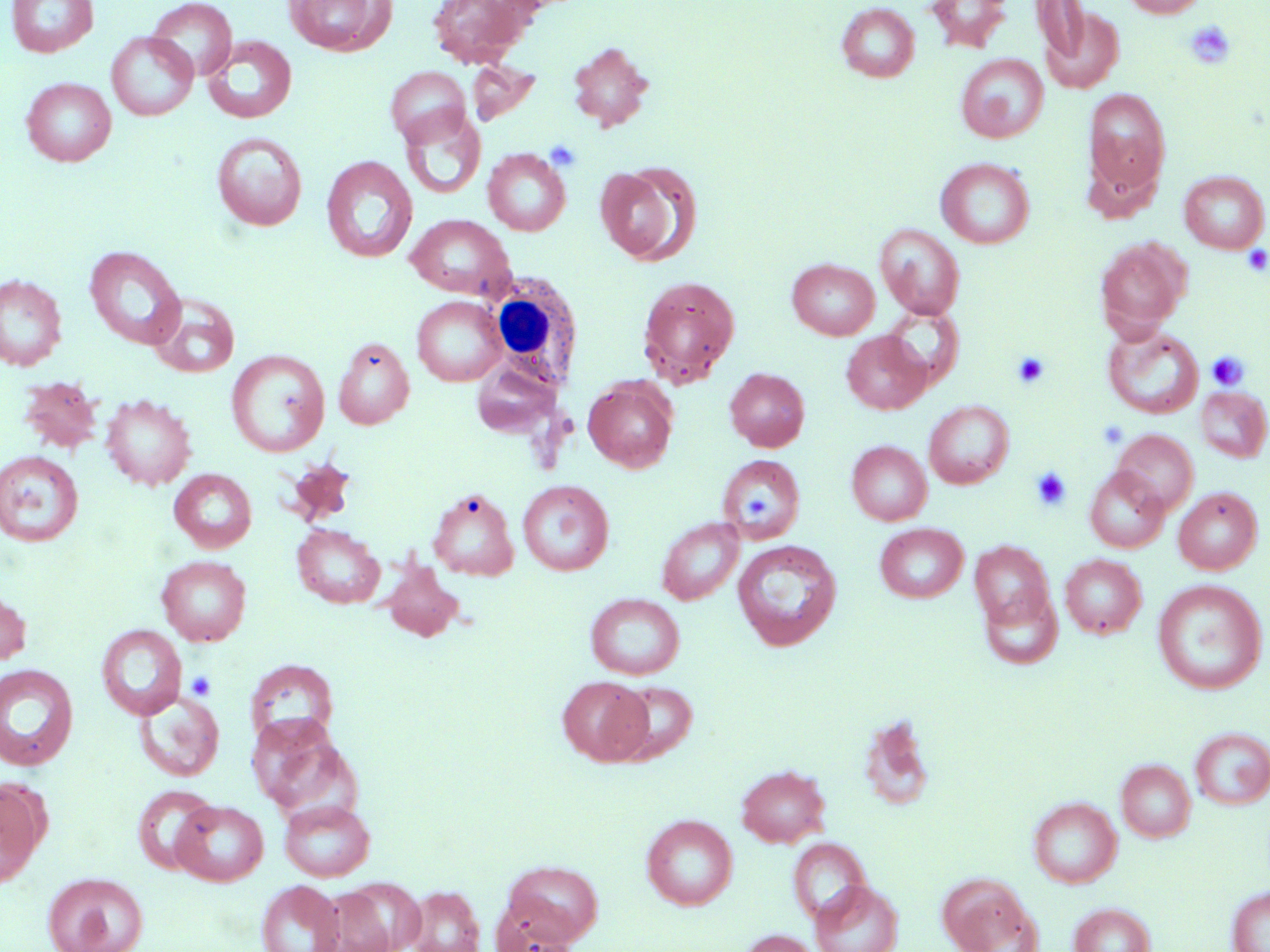

slide-level diagnosis = negative for blood parasites
preparation = thin blood film
white blood cell locations = approximate bounding boxes as (x1,y1)-(x2,y2) corner pairs in pixels: (478,269)-(584,391)
field of view = single
stain = May-Grünwald-Giemsa
uninfected red blood cell locations = approximate bounding boxes as (x1,y1)-(x2,y2) corner pairs in pixels: (6,0)-(98,57), (147,0)-(237,81), (284,0)-(395,56), (427,0)-(535,68), (926,0)-(1014,53), (1031,0)-(1091,64), (1123,0)-(1207,18), (836,2)-(920,82), (1037,4)-(1124,93), (106,32)-(198,121), (202,35)-(297,123), (567,41)-(654,132), (956,54)-(1048,143), (466,60)-(541,126), (385,66)-(471,147), (21,77)-(116,166), (1083,88)-(1171,203), (399,108)-(486,201), (211,132)-(307,231), (483,149)-(571,236), (321,156)-(417,263), (935,157)-(1035,248), (595,163)-(702,267), (1179,170)-(1269,253), (406,214)-(515,299), (875,224)-(965,320), (1095,239)-(1190,334), (84,245)-(186,350), (787,259)-(880,340), (0,274)-(66,370), (637,275)-(740,388), (148,294)-(240,378), (412,296)-(507,386), (881,304)-(965,388), (1103,324)-(1204,419), (842,331)-(931,414), (332,337)-(414,428), (226,349)-(330,457), (470,359)-(565,439), (725,367)-(810,451), (18,375)-(103,454), (583,377)-(678,473), (1195,386)-(1270,463), (100,393)-(196,490), (924,400)-(1014,489), (1112,429)-(1199,515), (847,440)-(932,525), (0,450)-(84,547), (717,454)-(806,544), (1084,467)-(1170,553), (169,469)-(257,553), (517,479)-(614,576), (1173,487)-(1262,574), (427,488)-(519,580), (657,517)-(744,604), (292,523)-(385,608), (875,523)-(968,603), (733,540)-(842,651), (969,540)-(1055,633), (1060,554)-(1147,638), (156,555)-(252,645), (380,559)-(466,642), (1152,579)-(1267,694), (979,584)-(1064,670), (0,591)-(31,665), (585,593)-(686,680), (97,624)-(187,720), (245,658)-(339,746), (0,664)-(79,770), (557,676)-(652,765), (612,680)-(698,763), (134,692)-(224,782), (245,712)-(356,817), (856,723)-(938,811), (1190,727)-(1270,810), (1116,758)-(1196,842), (736,764)-(830,847), (0,781)-(47,888), (132,785)-(219,874), (1028,797)-(1122,887), (279,799)-(375,882), (172,800)-(269,886), (641,814)-(737,909), (787,837)-(872,925), (500,861)-(604,945), (42,872)-(147,952), (937,873)-(1039,952), (811,880)-(903,952), (257,881)-(344,952), (405,885)-(485,952), (314,886)-(398,952), (1227,887)-(1270,952), (489,897)-(580,952), (1069,902)-(1156,952), (738,929)-(822,952)
platelet locations = approximate bounding boxes as (x1,y1)-(x2,y2) corner pairs in pixels: (1184,21)-(1236,69), (544,139)-(582,171), (1242,245)-(1270,276), (1012,351)-(1050,389), (1206,351)-(1250,390), (1097,419)-(1129,449), (1030,467)-(1072,511), (741,490)-(775,519), (185,670)-(216,700)
modality = light microscopy
magnification = 1000x
image size = 1270×952 pixels